Classify this cell by malaria status.
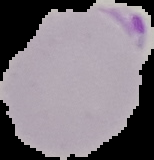

It is parasitized.

Summary:
  - Image size: 154×160 pixels
  - Preparation: thin blood film
  - Image type: segmented cell region with the area outside set to black